Point out leukocytes.
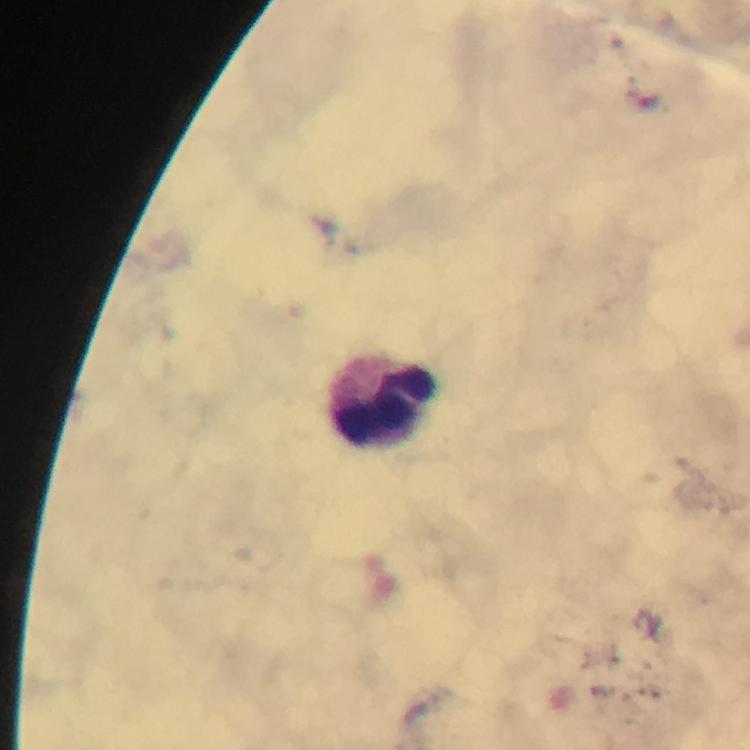
Approximate centers as (x, y) in pixels.
Leukocytes: (388, 403).

image size = 750×750 pixels
stain = Giemsa
preparation = thick smear
context = from a malaria diagnostic workup
immersion oil = used
magnification = 100x
capture = smartphone photograph through a microscope
Plasmodium parasites = none detected
cropped from = one field of view